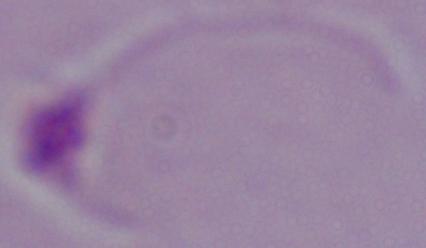
magnification = 1000x
identification = Leishmania
modality = photomicrograph